Give the extent of all Plasmodium parasites.
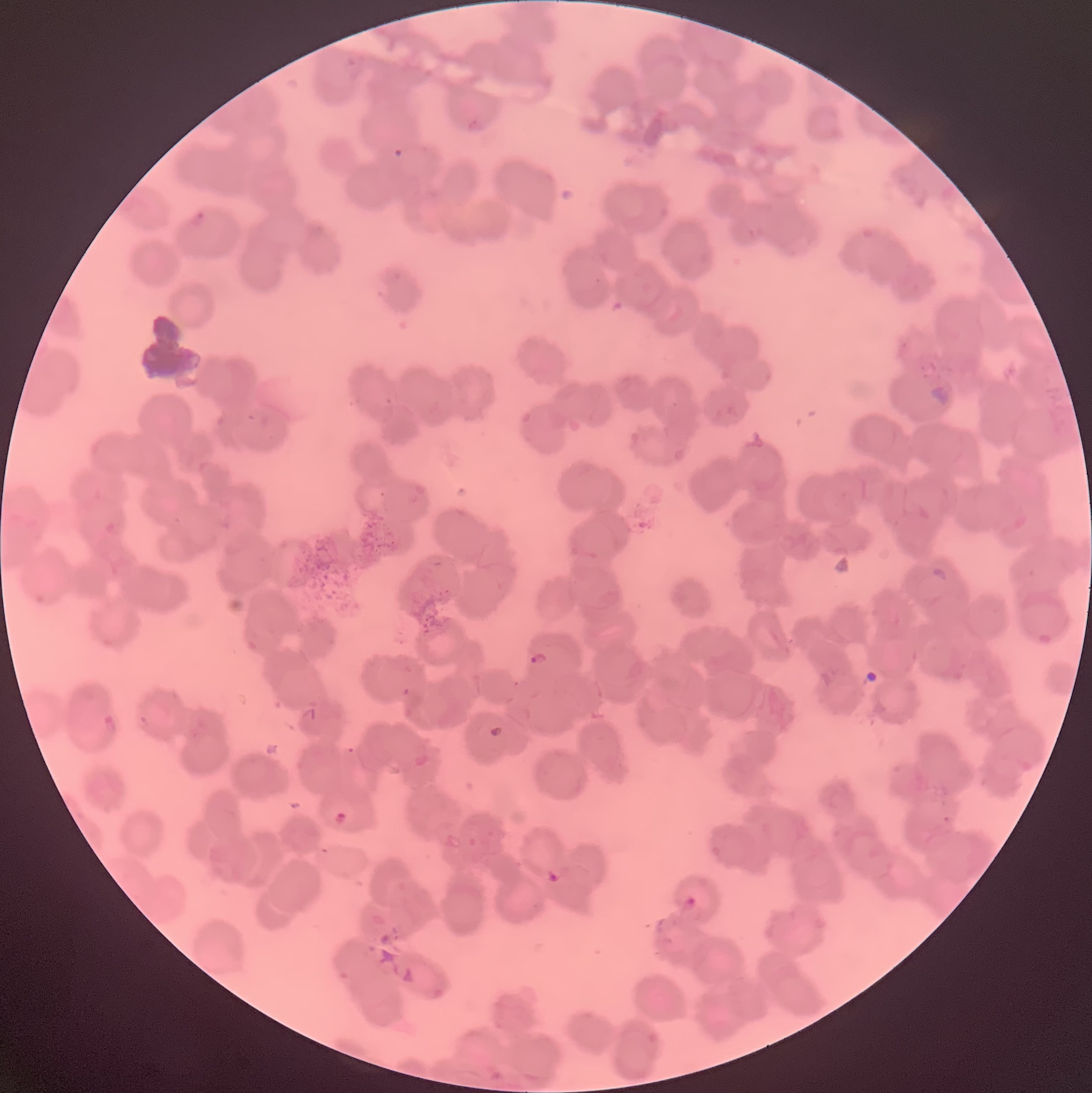

Approximate bounding boxes as [x1, y1, x2, y2] in pixels.
Plasmodium parasites: [467, 117, 484, 133], [392, 148, 405, 160], [188, 210, 207, 230], [927, 383, 956, 407], [529, 651, 549, 666], [102, 714, 119, 736], [489, 725, 504, 738], [334, 811, 347, 826], [546, 867, 563, 884], [682, 896, 697, 913].

preparation = thin blood smear
image size = 1092×1093 pixels
red blood cell morphology = rouleaux formation
modality = light microscopy